Comment on the morphology of the red blood cells.
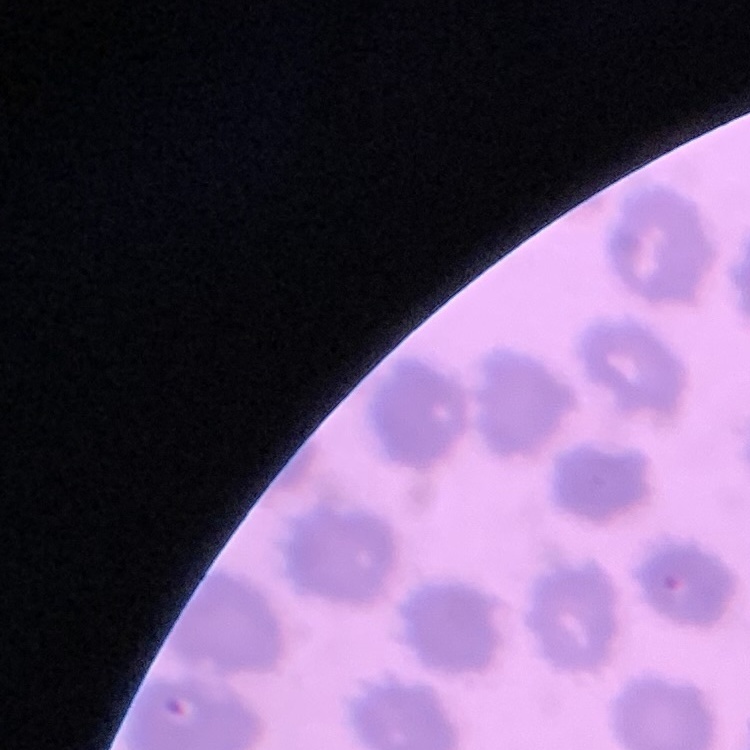

They show no rouleaux formation.

{
  "stain": "Field's or Giemsa",
  "image_type": "square crop of a larger photomicrograph",
  "preparation": "thin blood film"
}